Locate and identify every blood parasite.
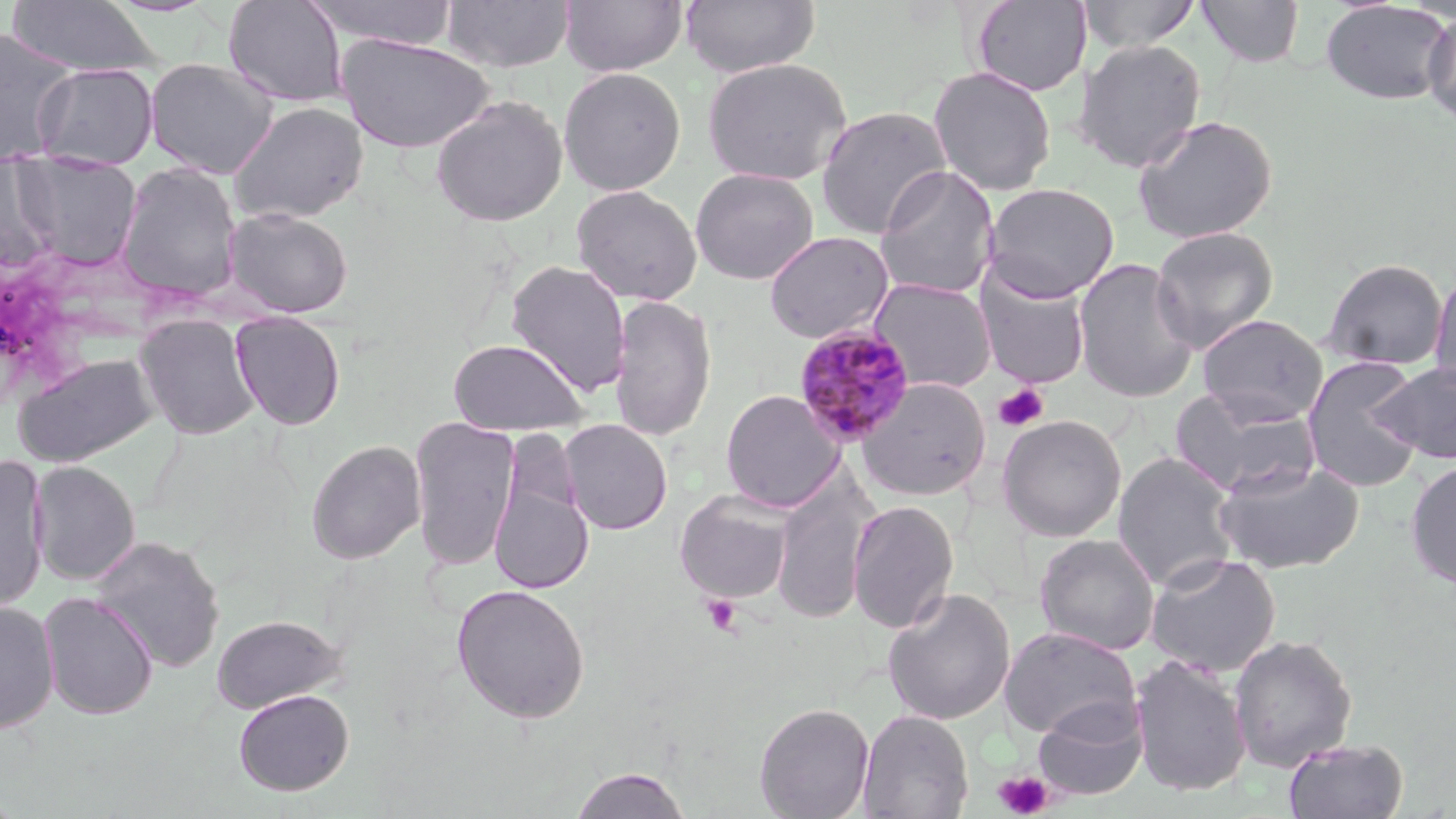
Approximate bounding boxes as [x1, y1, x2, y2] in pixels.
Plasmodium malariae-infected red blood cells: [793, 325, 916, 447].
No Plasmodium falciparum, Plasmodium ovale, Plasmodium vivax, Babesia divergens, or Trypanosoma brucei observed.

Summary:
  - Platelet locations: [993, 384, 1049, 432], [702, 594, 742, 636], [993, 769, 1054, 819]
  - Uninfected red blood cell locations: [222, 0, 349, 107], [305, 0, 459, 48], [440, 0, 575, 72], [560, 0, 688, 77], [681, 0, 820, 77], [1078, 0, 1202, 54], [1195, 0, 1305, 67], [6, 1, 160, 77], [970, 1, 1091, 96], [1320, 1, 1453, 105], [1422, 8, 1456, 127], [0, 29, 78, 161], [337, 34, 494, 153], [1074, 39, 1207, 173], [145, 58, 279, 179], [701, 58, 852, 186], [32, 63, 158, 169], [928, 66, 1057, 197], [557, 67, 686, 196], [430, 94, 568, 227], [227, 102, 369, 225], [815, 105, 953, 239], [1132, 114, 1278, 244], [12, 157, 142, 271], [0, 161, 57, 272], [114, 162, 243, 303], [873, 165, 1001, 301], [690, 168, 818, 285], [983, 182, 1119, 301], [571, 184, 703, 306], [222, 206, 355, 318], [1150, 225, 1279, 353], [763, 230, 895, 344], [1073, 257, 1200, 403], [1321, 257, 1449, 370], [505, 260, 632, 399], [1429, 265, 1456, 397], [974, 269, 1092, 389], [867, 278, 997, 394], [609, 294, 717, 443], [230, 311, 346, 430], [135, 314, 260, 440], [1197, 314, 1328, 425], [448, 338, 588, 436], [12, 353, 158, 467], [1301, 355, 1425, 493], [1373, 360, 1456, 464], [857, 377, 991, 500], [1169, 388, 1322, 499], [719, 389, 844, 513], [996, 414, 1127, 542], [409, 415, 521, 571], [558, 418, 673, 535], [306, 439, 426, 565], [489, 440, 594, 600], [1113, 451, 1241, 592], [0, 453, 50, 613], [1215, 458, 1364, 574], [1405, 459, 1456, 590], [29, 460, 140, 586], [771, 471, 878, 625], [675, 490, 795, 604], [847, 499, 959, 634], [1034, 533, 1161, 655], [90, 535, 225, 673], [1145, 551, 1282, 677], [451, 583, 591, 724], [882, 587, 1016, 726], [38, 592, 158, 720], [0, 602, 59, 733], [211, 614, 347, 714], [999, 624, 1141, 741], [1228, 634, 1357, 772], [1130, 654, 1252, 797], [233, 688, 354, 796], [1032, 698, 1148, 801], [754, 702, 875, 819], [857, 708, 974, 819], [1283, 738, 1409, 819], [567, 765, 694, 819]
  - Slide-level diagnosis: Plasmodium malariae
  - Modality: optical microscopy
  - Field of view: one of a larger specimen
  - Image size: 1456×819 pixels
  - Stain: May-Grünwald-Giemsa
  - Magnification: 1000x
  - Preparation: thin blood film